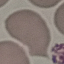 Result: negative for malaria parasites. Cell patch, automatically extracted from a larger field of view and resized to 64 × 64 pixels. Giemsa-stained preparation. Photographed with a smartphone camera at the microscope eyepiece. Thin smear of blood.